Classify this cell by malaria status.
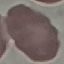
Uninfected.

Photographed with a smartphone camera at the microscope eyepiece. Thin blood film. Automatically extracted cell patch, resized to 64 × 64 pixels. Giemsa-stained preparation.